Report the malaria status of this cell.
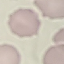
Uninfected.

capture: smartphone through the microscope eyepiece
preparation: thin smear
stain: Giemsa
image_type: automatically extracted cell patch, resized to 64 × 64 pixels